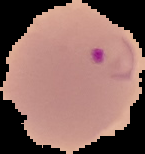
preparation = thin blood film
image type = segmented cell region on a black background
image size = 145×154 pixels
result = Plasmodium parasites identified